Outline every leukocyte.
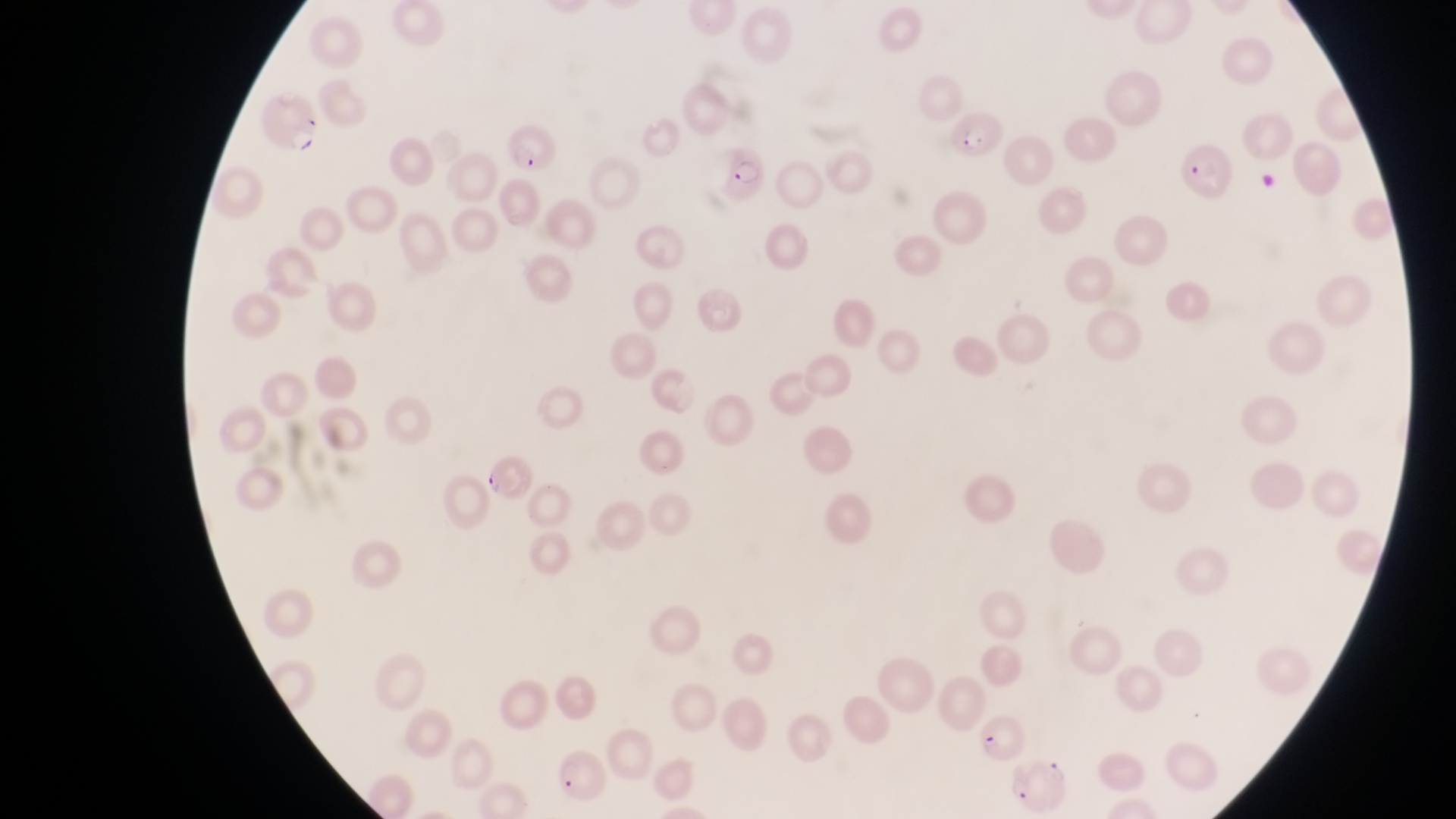
No leukocytes observed.

Approximate bounding boxes as (left, top, right, bottom) in pixels. Parasitised red blood cell locations: (254, 96, 325, 160), (948, 112, 1004, 159), (502, 121, 558, 177), (1182, 139, 1234, 203), (723, 146, 772, 207), (479, 457, 532, 500), (980, 714, 1026, 760), (552, 753, 610, 803), (1004, 756, 1073, 817). One field of view. Thin blood smear. At a magnification of 1000x. Captured by a smartphone held over the eyepiece of an Olympus CX-23 microscope. Sample from Uganda. Image is 1456×819 pixels.